Locate platelets.
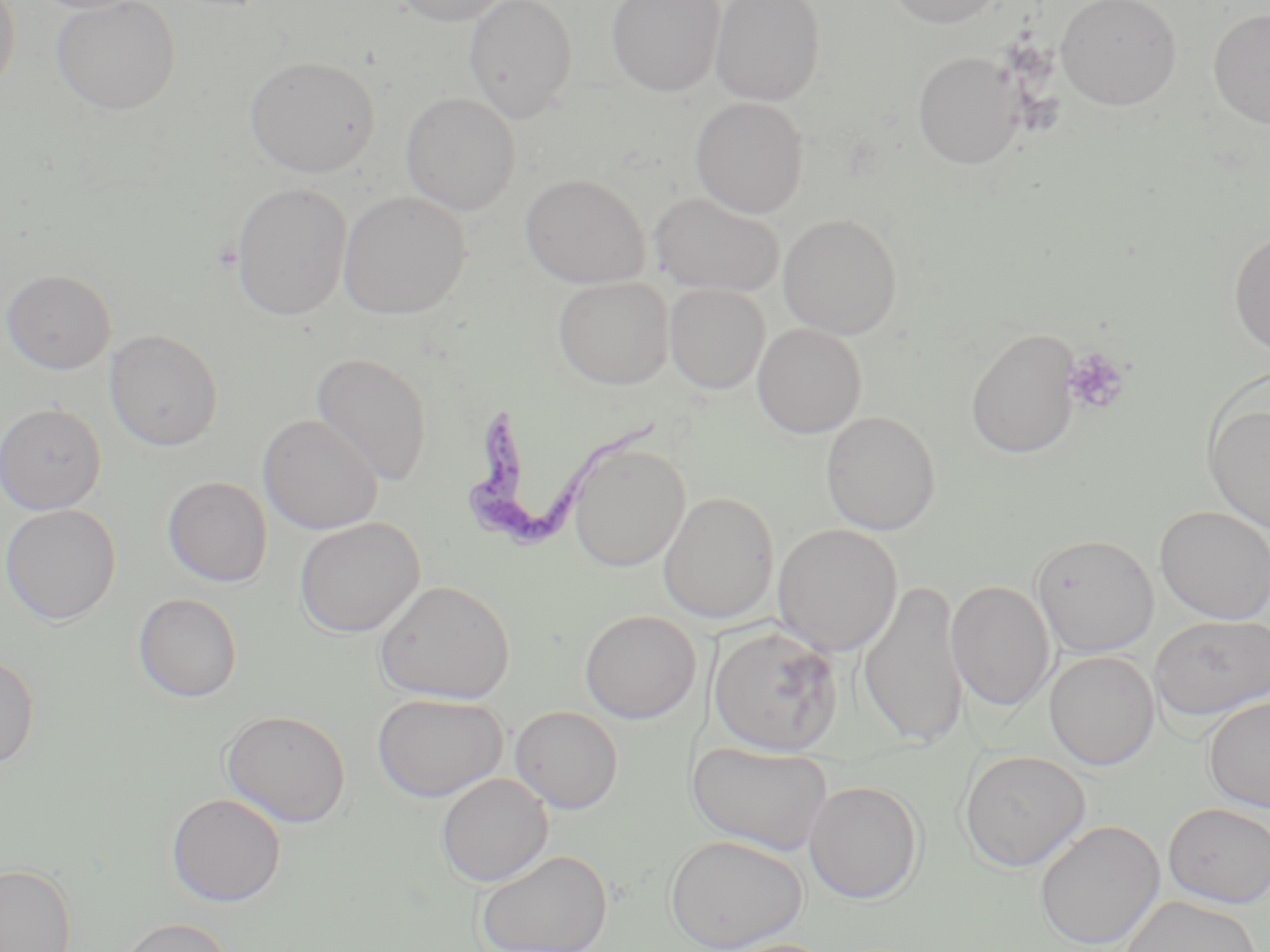
Approximate bounding boxes as [x1, y1, x2, y2] in pixels.
Platelets: [1061, 348, 1130, 415].

Trypanosoma brucei locations: [463, 404, 673, 553]. Uninfected red blood cell locations: [0, 0, 21, 98], [51, 0, 182, 115], [388, 0, 515, 26], [463, 0, 578, 122], [607, 0, 724, 96], [710, 0, 825, 105], [884, 0, 1006, 28], [1055, 0, 1182, 110], [1208, 8, 1270, 129], [913, 51, 1024, 169], [244, 55, 380, 177], [401, 92, 521, 215], [690, 96, 808, 217], [520, 173, 650, 289], [231, 182, 352, 321], [338, 190, 471, 319], [650, 192, 784, 297], [778, 213, 902, 340], [1228, 228, 1270, 357], [1, 269, 117, 374], [553, 277, 674, 389], [664, 284, 770, 394], [753, 323, 866, 438], [966, 328, 1080, 458], [104, 329, 224, 451], [310, 352, 433, 486], [1203, 398, 1270, 533], [0, 402, 107, 515], [821, 410, 941, 536], [258, 413, 383, 534], [569, 440, 689, 572], [162, 476, 272, 587], [658, 491, 779, 624], [0, 504, 121, 625], [1155, 506, 1270, 624], [294, 516, 425, 637], [773, 524, 902, 656], [1031, 534, 1159, 658], [858, 577, 969, 747], [375, 579, 515, 703], [946, 580, 1056, 711], [133, 593, 243, 702], [579, 609, 701, 724], [1149, 614, 1270, 721], [708, 625, 842, 756], [1044, 650, 1160, 771], [0, 653, 40, 770], [372, 692, 508, 801], [1203, 696, 1270, 812], [510, 705, 624, 814], [220, 708, 352, 827], [688, 741, 834, 855], [958, 749, 1091, 871], [436, 772, 553, 887], [804, 780, 924, 904], [166, 792, 287, 907], [1162, 802, 1270, 908], [1034, 818, 1165, 950], [665, 834, 808, 951], [475, 848, 614, 952], [0, 862, 77, 952], [1121, 895, 1262, 952], [115, 916, 234, 952], [711, 938, 840, 952]. Slide-level diagnosis: Trypanosoma brucei. Light microscopy. Image is 1270×952 pixels. 1000x magnification. One field of a larger specimen. Thin blood smear. May-Grünwald-Giemsa stain.